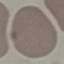
malaria status = uninfected
capture = smartphone camera at the microscope eyepiece
stain = Giemsa
image type = automatically extracted cell patch, resized to 64 × 64 pixels
preparation = thin smear